Identify the parasite.
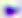

This is Toxoplasma gondii.

{
  "modality": "micrograph",
  "magnification": "400x"
}